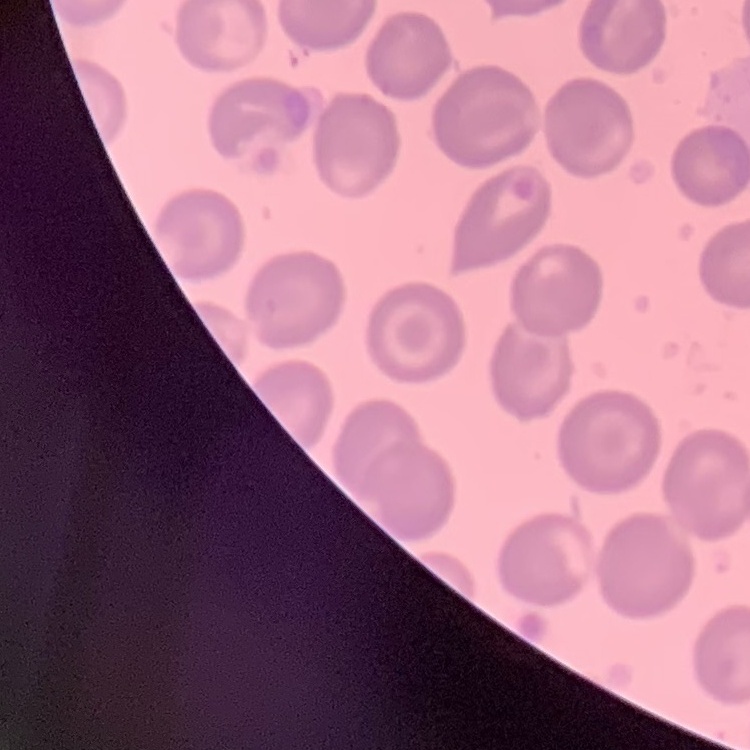
erythrocyte morphology = no rouleaux formation
preparation = thin peripheral smear
stain = Field's or Giemsa
image type = square crop of a larger photomicrograph